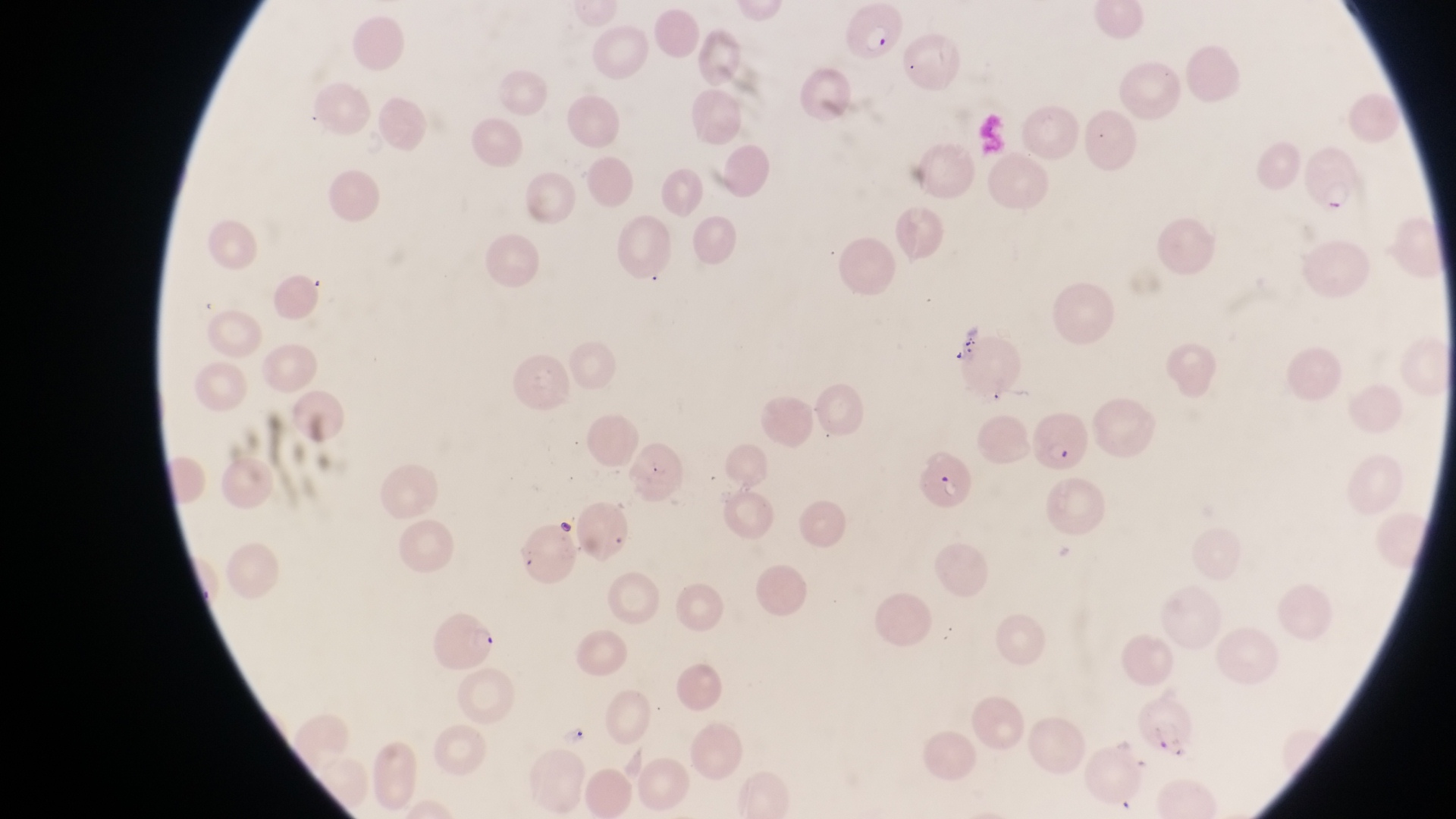
Approximate bounding boxes as {left, top, right, bottom} in pixels.
Summary:
  - Artifact (platelet-like body, stain precipitate, or debris) locations: {552, 516, 578, 545}
  - Parasitised red blood cell locations: {842, 3, 905, 62}, {1304, 139, 1364, 215}, {1033, 413, 1092, 471}, {920, 449, 978, 508}, {425, 611, 502, 674}
  - Image size: 1456×819 pixels
  - Field of view: single
  - Country: Uganda
  - Preparation: thin blood smear
  - Magnification: 1000x
  - Capture: smartphone photograph through the eyepiece of an Olympus CX-23 microscope